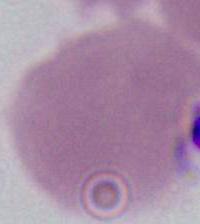
modality = micrograph
magnification = 1000x
identification = red blood cell